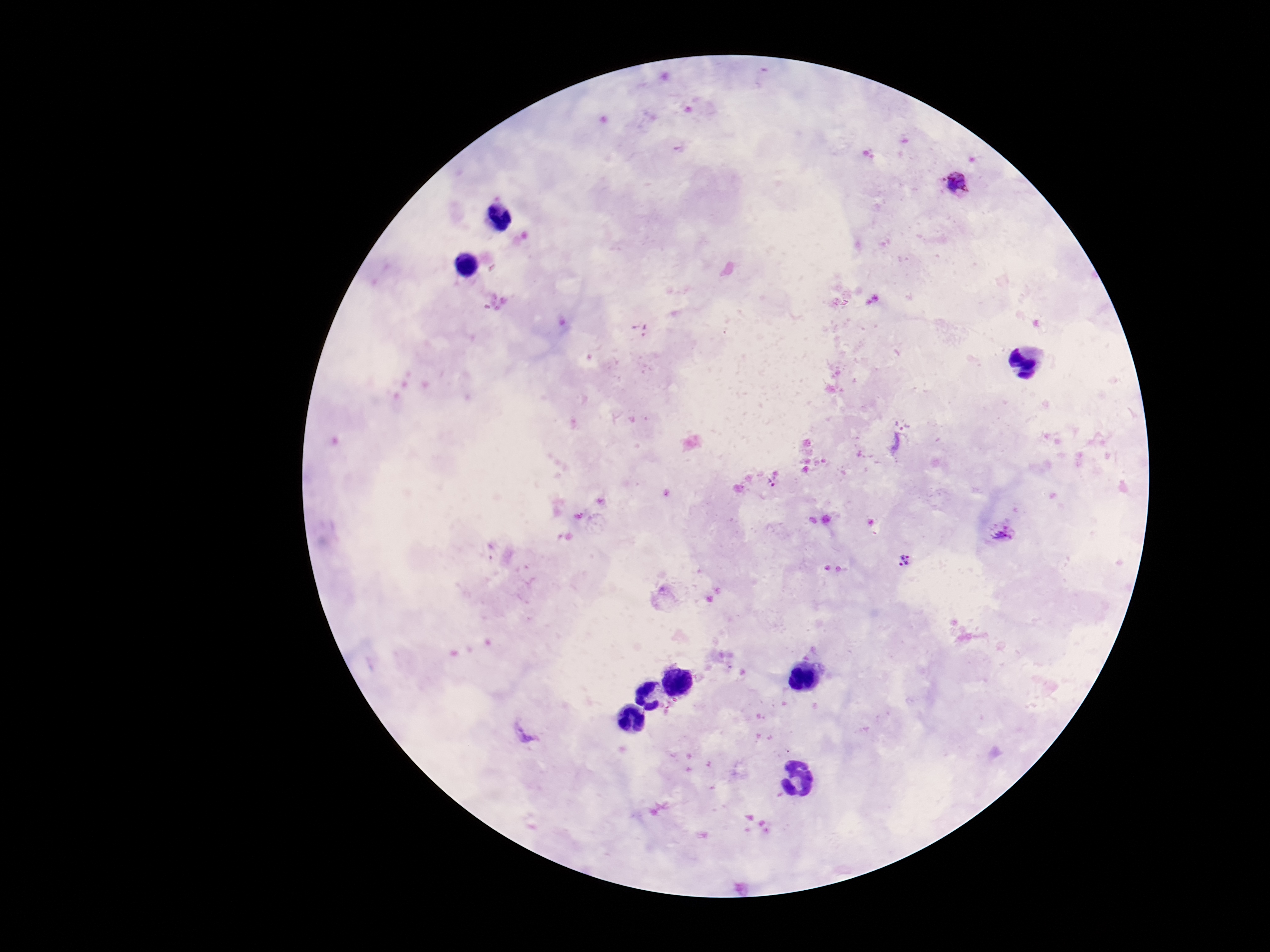
Approximate centers as (x, y) in pixels.
Summary:
  - Plasmodium parasite locations: (957, 180), (644, 328), (901, 438), (772, 481), (1005, 531), (492, 554), (905, 560), (523, 730)
  - Field of view: one from this slide
  - Magnification: 100x
  - Image size: 1270×952 pixels
  - Capture: smartphone camera through the microscope eyepiece
  - Patient malaria status: infected
  - Stain: Giemsa
  - Preparation: thick peripheral-blood smear